Describe the morphology of the erythrocytes.
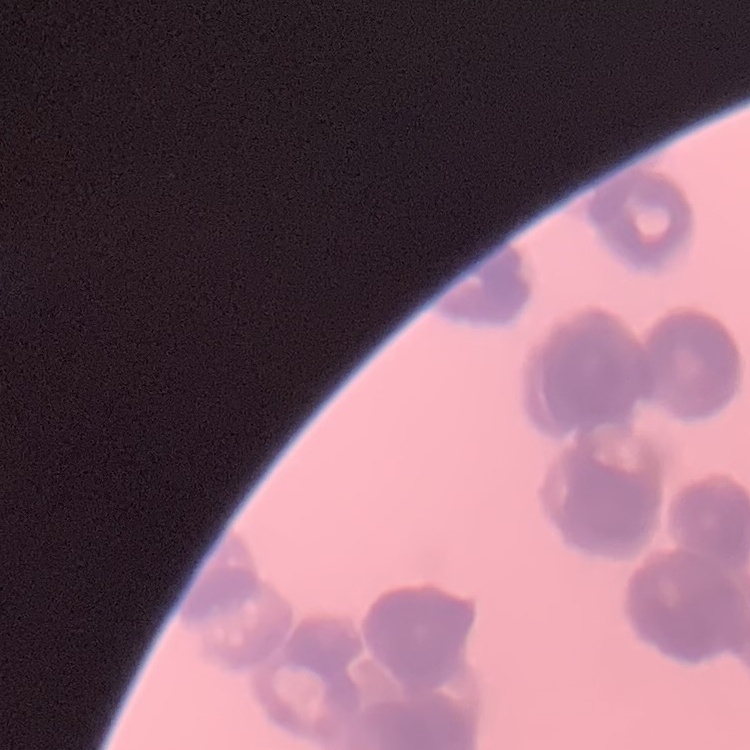
They show rouleaux formation.

preparation = thin blood smear
image type = one tile cut from a larger photomicrograph
stain = Field's or Giemsa